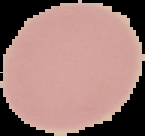 From a thin blood film. Result: no malaria parasites seen. Image is 145×136 pixels. Segmented cell region on a black background.